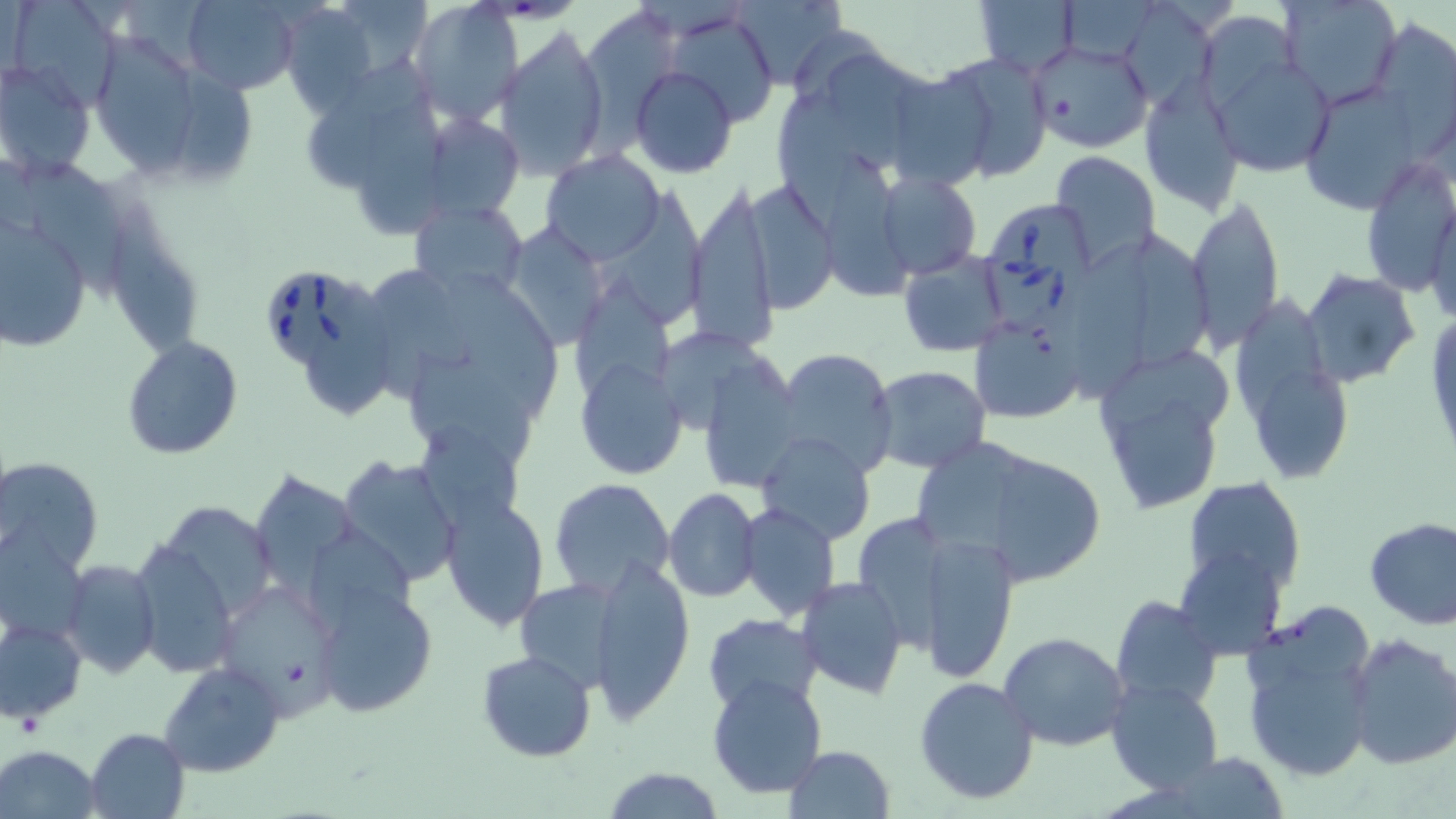
slide_level_diagnosis: Babesia divergens
modality: light microscopy
babesia_divergens_infected_red_blood_cell_locations: 'approximate bounding boxes as (x1,y1)-(x2,y2) corner pairs in pixels: (987,204)-(1096,329), (268,275)-(372,374)'
magnification: 1000x
field_of_view: single
image_size: 1456×819 pixels
preparation: thin blood smear
uninfected_red_blood_cell_locations: 'approximate bounding boxes as (x1,y1)-(x2,y2) corner pairs in pixels: (4,0)-(121,108), (733,0)-(846,89), (1060,0)-(1162,65), (1121,0)-(1217,111), (1276,0)-(1403,110), (181,1)-(300,93), (974,1)-(1078,75), (409,2)-(523,127), (280,4)-(380,118), (578,5)-(687,132), (665,8)-(780,127), (1370,20)-(1455,150), (494,26)-(611,179), (786,29)-(895,101), (95,35)-(203,174), (1026,37)-(1153,154), (1147,37)-(1306,205), (1204,45)-(1335,178), (927,51)-(1054,182), (829,55)-(911,177), (0,58)-(97,181), (306,63)-(427,199), (630,66)-(739,179), (175,69)-(254,178), (896,73)-(993,191), (1138,75)-(1243,214), (1297,79)-(1436,212), (778,81)-(857,234), (356,92)-(445,241), (419,111)-(524,221), (19,149)-(125,303), (539,149)-(666,265), (1049,151)-(1162,272), (1356,154)-(1456,300), (875,167)-(982,280), (739,179)-(836,313), (688,185)-(778,357), (1424,191)-(1455,330), (1187,194)-(1284,349), (409,198)-(529,302), (104,199)-(202,363), (0,216)-(94,353), (499,223)-(612,350), (1073,231)-(1155,397), (1133,231)-(1215,370), (898,252)-(1009,356), (368,266)-(477,400), (1301,270)-(1420,389), (454,274)-(561,414), (304,284)-(389,418), (1238,290)-(1328,418), (1424,306)-(1456,466), (968,320)-(1085,424), (122,336)-(242,459), (771,348)-(898,481), (410,352)-(535,467), (702,358)-(802,494), (574,359)-(687,481), (1104,359)-(1238,437), (869,365)-(993,475), (1258,367)-(1347,484), (1114,399)-(1214,511), (415,425)-(526,530), (755,432)-(876,546), (915,437)-(1040,562), (338,453)-(464,587), (1,456)-(103,576), (998,461)-(1107,586), (252,471)-(357,594), (1182,476)-(1308,596), (548,478)-(676,601), (665,488)-(761,601), (442,499)-(551,630), (738,504)-(841,619), (850,512)-(966,662), (1363,516)-(1456,630), (916,527)-(1018,681), (0,529)-(88,647), (130,536)-(242,677), (1174,547)-(1287,659), (591,556)-(693,722), (60,559)-(160,678), (794,576)-(908,699), (513,579)-(625,693), (314,581)-(439,717), (220,583)-(344,709), (1112,596)-(1223,712), (1239,608)-(1373,679), (701,614)-(823,712), (1,616)-(86,724), (997,631)-(1130,752), (1344,633)-(1456,770), (477,650)-(597,763), (158,660)-(286,778), (1251,662)-(1369,777), (706,675)-(827,799), (914,676)-(1040,806), (1105,677)-(1223,795), (84,727)-(190,819), (1,745)-(101,816), (783,745)-(896,819), (1164,752)-(1288,818), (601,765)-(726,819)'
stain: May-Grünwald-Giemsa